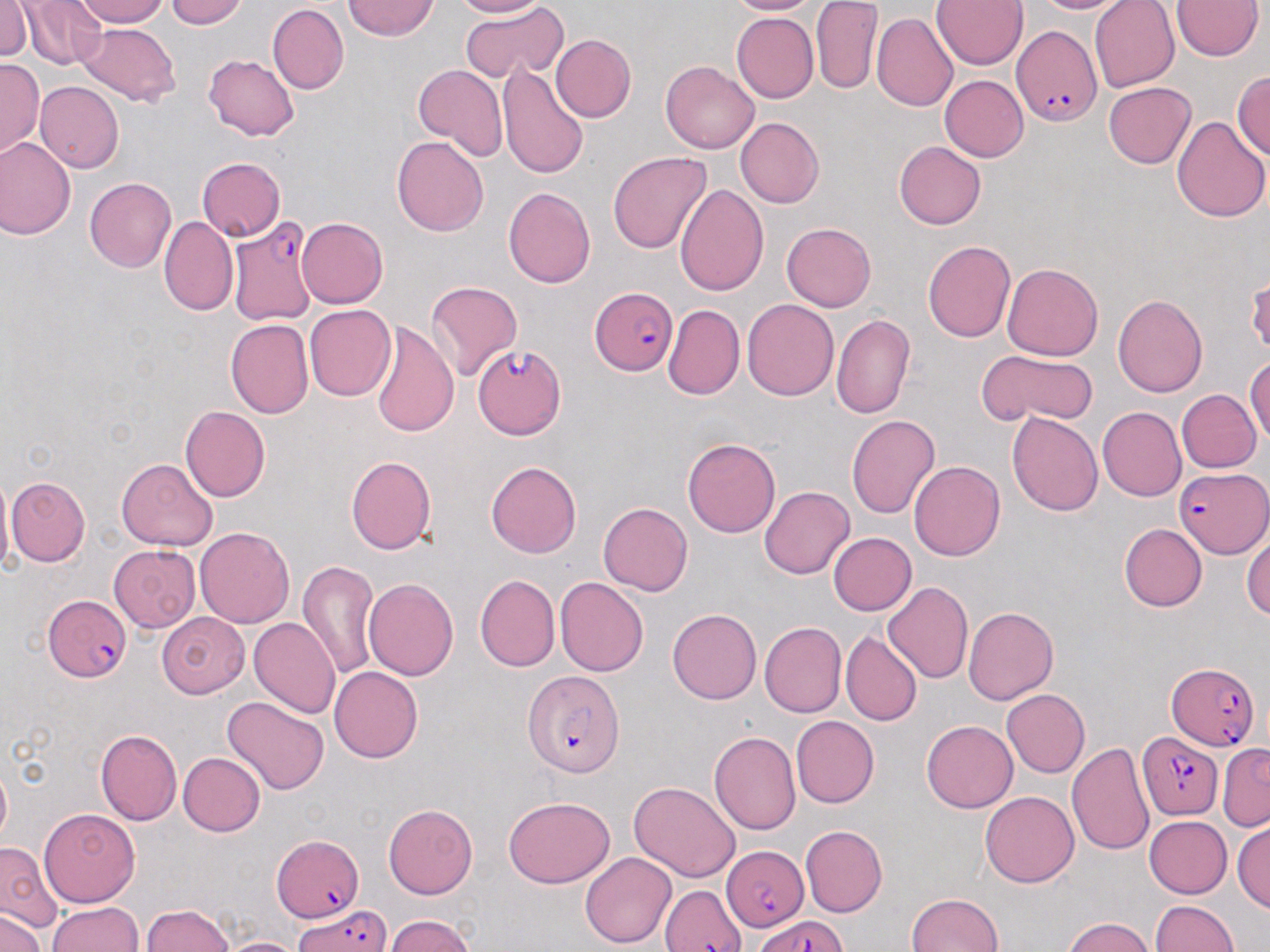

Approximate bounding boxes as [x1, y1, x2, y2] in pixels. Plasmodium falciparum-infected red blood cell locations: [1012, 25, 1102, 122], [229, 217, 319, 325], [590, 288, 680, 376], [472, 345, 565, 438], [1175, 465, 1270, 558], [44, 596, 131, 684], [1167, 660, 1261, 749], [521, 669, 627, 779], [1137, 729, 1224, 820], [273, 833, 367, 922], [720, 835, 806, 939], [657, 882, 746, 951], [294, 903, 389, 950], [752, 916, 850, 952]. Uninfected red blood cell locations: [0, 0, 32, 62], [22, 0, 107, 71], [67, 0, 175, 28], [162, 0, 247, 29], [343, 0, 440, 42], [454, 0, 547, 19], [727, 0, 819, 17], [811, 0, 880, 92], [931, 0, 1025, 71], [1021, 0, 1128, 17], [1088, 0, 1180, 92], [1173, 0, 1262, 62], [457, 4, 568, 84], [266, 5, 348, 94], [730, 12, 818, 103], [871, 13, 957, 111], [73, 20, 182, 106], [551, 33, 636, 121], [201, 52, 297, 143], [2, 60, 41, 155], [499, 60, 589, 180], [661, 61, 757, 153], [412, 65, 507, 161], [1234, 67, 1270, 167], [941, 75, 1032, 162], [1103, 81, 1195, 169], [37, 83, 124, 172], [1173, 114, 1268, 223], [736, 119, 824, 206], [1, 137, 76, 238], [392, 137, 488, 237], [895, 140, 987, 229], [608, 151, 711, 254], [197, 156, 285, 241], [85, 177, 177, 272], [674, 181, 768, 295], [502, 186, 595, 288], [160, 215, 239, 316], [295, 217, 389, 310], [782, 222, 877, 312], [923, 240, 1015, 342], [1001, 263, 1103, 361], [1248, 271, 1270, 361], [426, 282, 521, 382], [1112, 293, 1209, 395], [740, 297, 838, 399], [662, 304, 745, 398], [305, 305, 396, 401], [831, 314, 916, 419], [227, 320, 314, 419], [371, 321, 460, 439], [978, 347, 1097, 428], [1245, 357, 1269, 446], [1175, 390, 1259, 473], [181, 405, 270, 502], [1098, 407, 1188, 500], [1007, 409, 1101, 516], [845, 414, 940, 518], [683, 436, 782, 538], [345, 455, 435, 555], [117, 459, 215, 552], [909, 460, 1006, 560], [486, 461, 582, 557], [0, 472, 16, 578], [7, 474, 93, 567], [760, 485, 852, 580], [597, 501, 691, 596], [1120, 524, 1206, 612], [195, 527, 295, 628], [1244, 529, 1270, 623], [829, 532, 917, 615], [109, 545, 200, 634], [298, 560, 380, 679], [473, 575, 558, 673], [556, 577, 649, 676], [362, 578, 460, 681], [884, 581, 973, 685], [962, 605, 1059, 705], [669, 607, 763, 704], [156, 611, 248, 698], [248, 615, 339, 718], [760, 621, 846, 715], [841, 630, 922, 727], [328, 663, 422, 759], [1003, 689, 1091, 775], [222, 696, 330, 795], [791, 717, 879, 807], [921, 721, 1017, 812], [95, 729, 180, 824], [709, 731, 799, 836], [1068, 740, 1157, 855], [1219, 744, 1269, 832], [179, 752, 265, 836], [0, 763, 12, 849], [630, 781, 740, 880], [980, 791, 1077, 887], [503, 796, 616, 887], [383, 802, 479, 897], [39, 804, 139, 903], [1144, 816, 1231, 899], [1233, 822, 1269, 915], [800, 826, 888, 914], [1, 844, 55, 928], [580, 851, 675, 948], [904, 891, 1008, 952], [46, 902, 146, 952], [1151, 902, 1240, 952], [141, 903, 235, 952], [0, 913, 45, 952], [384, 915, 476, 952], [1061, 916, 1159, 952], [219, 935, 306, 952]. Slide-level diagnosis: Plasmodium falciparum. May-Grünwald-Giemsa-stained preparation. Single field of view. Thin blood film. Light microscopy. Image is 1270×952 pixels. Captured at 1000x magnification.